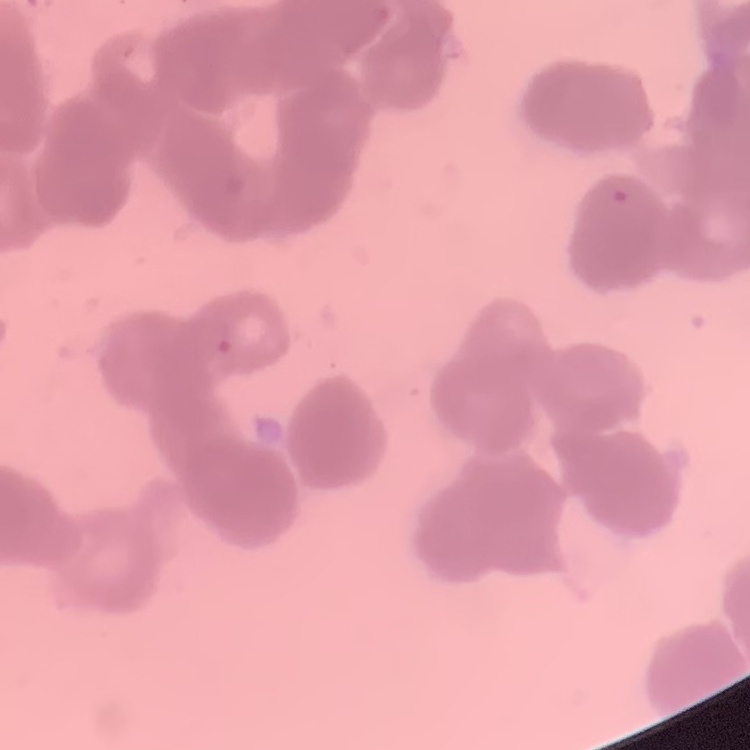
red_blood_cell_morphology: rouleaux formation
image_type: square crop of a larger photomicrograph
stain: Field's or Giemsa
preparation: thin blood smear